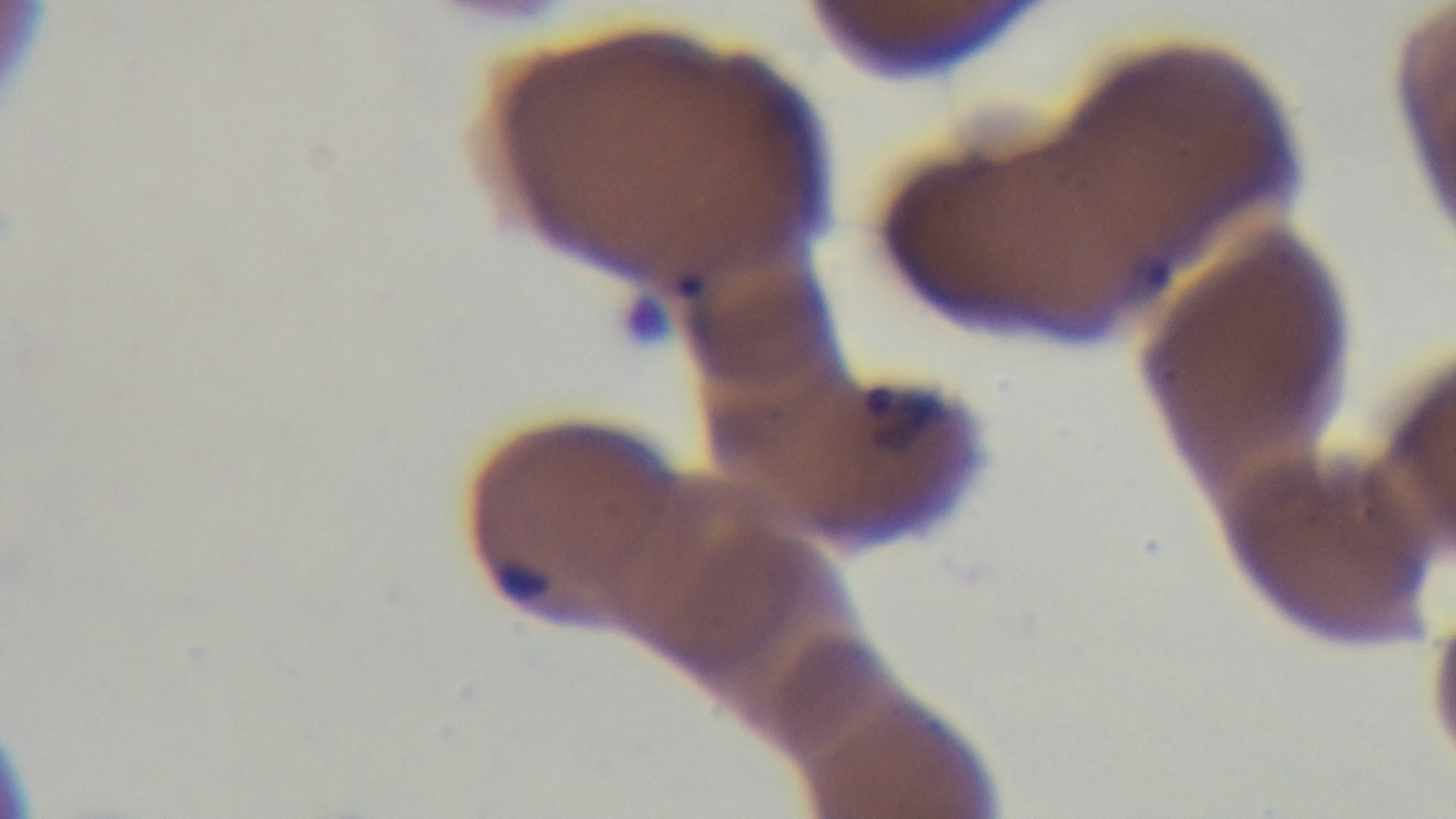
Giemsa-stained. Single field of view. Malaria status: infected. Preparation: thin blood film. Photomicrograph. Captured with a mounted 4K digital camera. Oil-immersion objective, 100x.